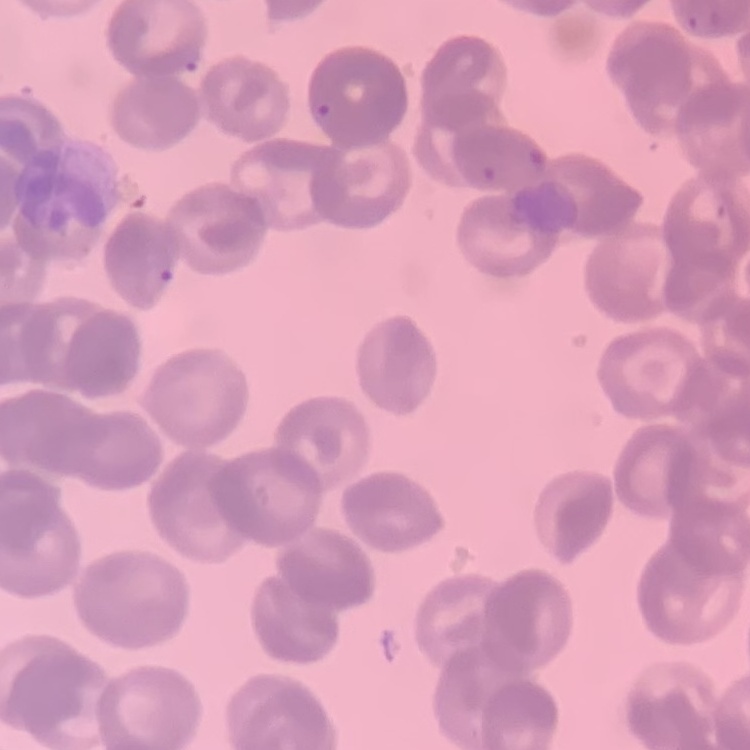
Summary:
  - Erythrocyte morphology: rouleaux formation
  - Stain: Field's or Giemsa
  - Image type: one tile cut from a larger photomicrograph
  - Preparation: thin blood film